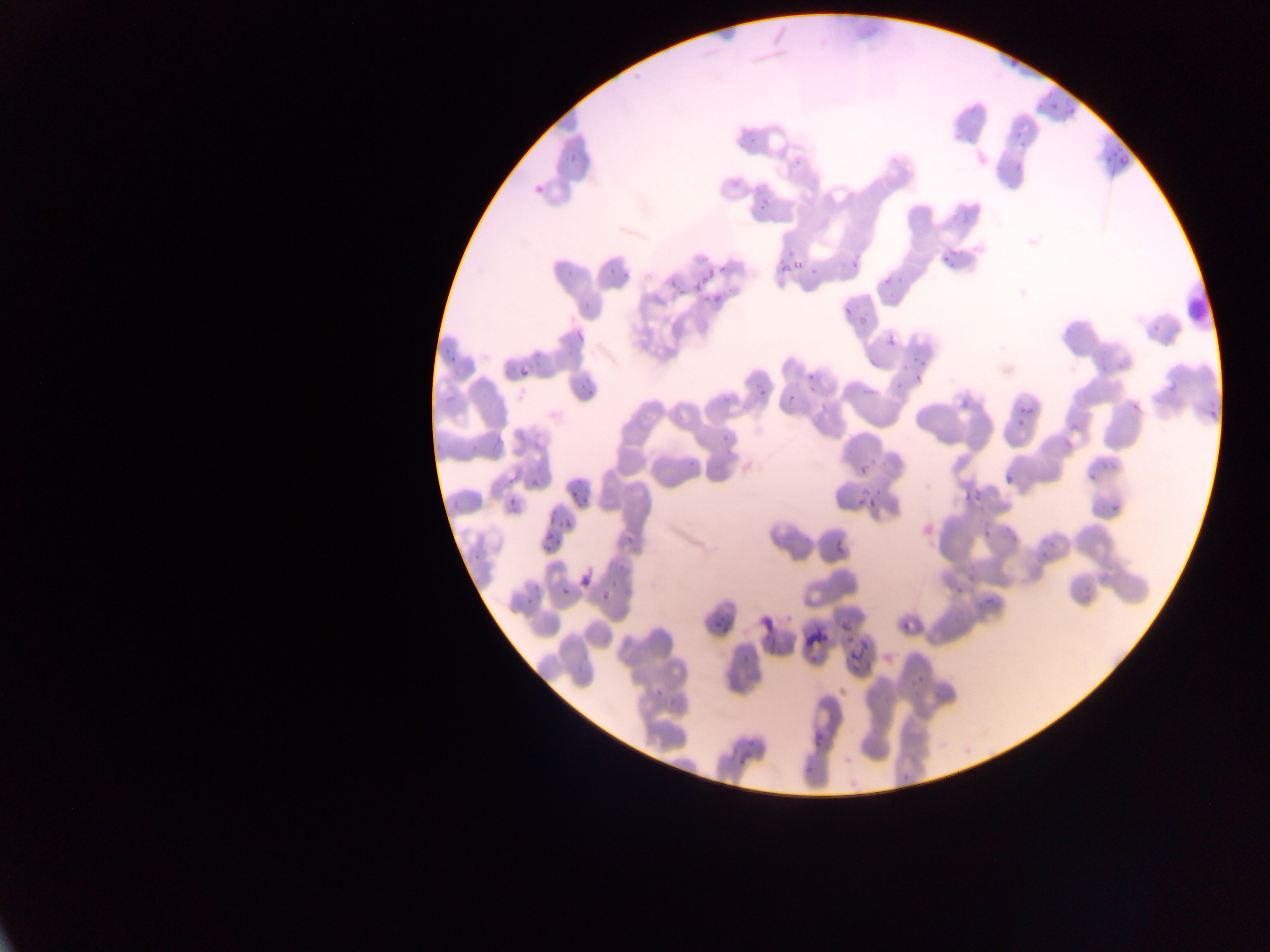

Approximate bounding boxes as left top right bottom in pixels.
Summary:
  - Plasmodium parasite locations: 1035 85 1069 113; 1062 95 1085 121; 1011 122 1030 151; 1097 142 1129 170; 564 148 578 163; 532 179 551 200; 758 201 770 213; 776 245 802 277; 937 247 957 268; 848 254 866 275; 716 262 731 277; 607 263 616 279; 804 267 824 282; 664 270 678 289; 880 270 898 291; 620 272 632 280; 695 275 705 291; 705 275 728 308; 839 294 862 316; 580 296 591 314; 859 310 874 330; 575 325 591 344; 885 334 900 349; 908 354 928 383; 515 358 531 378; 801 367 818 384; 579 370 595 391; 1157 379 1176 398; 753 380 772 403; 781 389 799 410; 1009 394 1034 430; 1131 402 1142 413; 1060 424 1078 452; 715 428 735 440; 860 449 872 463; 1091 457 1108 482; 682 458 696 472; 996 469 1019 490; 532 476 541 488; 503 478 513 488; 961 478 986 510; 579 480 595 501; 850 485 883 508; 568 486 578 498; 506 488 523 506; 1103 488 1132 516; 541 508 553 530; 560 516 576 529; 829 520 854 568; 623 523 638 544; 542 536 550 549; 551 536 563 546; 577 564 595 587; 952 568 975 597; 595 581 617 600; 555 582 575 598; 987 583 1004 604; 523 595 530 605; 710 614 731 632; 835 615 851 636; 902 626 908 634; 849 632 874 661; 739 648 752 669; 653 683 666 698; 810 727 828 755; 736 749 757 772; 804 754 821 779; 899 770 911 782
  - Preparation: thin blood film
  - Country: Ghana
  - Capture: mobile-phone photograph through a microscope
  - Field of view: single
  - Image size: 1270×952 pixels